Identify the cell.
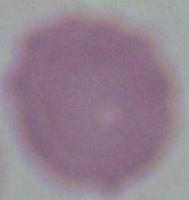

This is an erythrocyte.

Captured at 1000x magnification. Micrograph.